Classify this cell by malaria status.
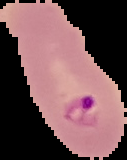

It is parasitized.

image size = 127×160 pixels
image type = segmented cell region on a black background
preparation = thin blood smear